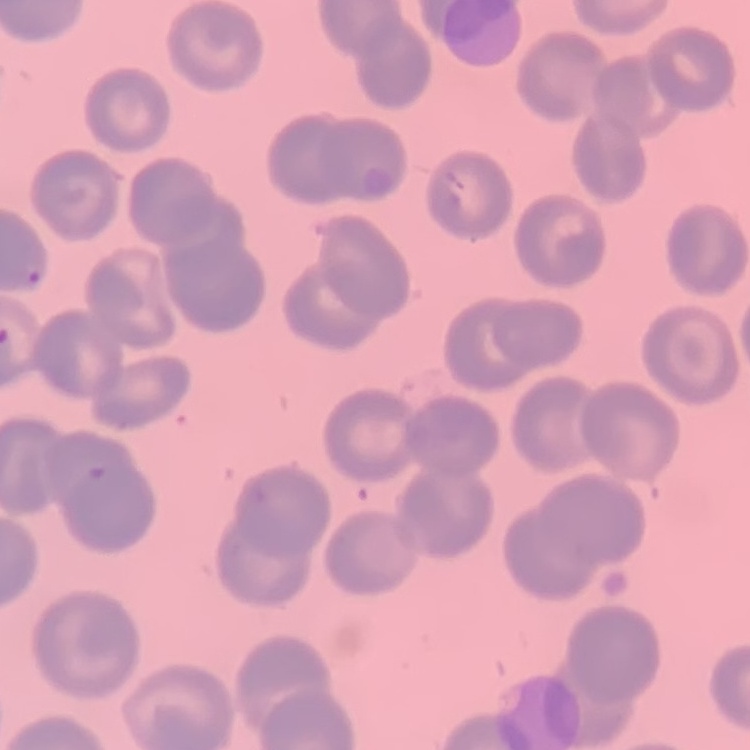
The red blood cells show no rouleaux formation. Stained with either Field's or Giemsa. Thin peripheral smear. One tile cut from a larger photomicrograph.